Give the extent of all Plasmodium malariae-infected red blood cells.
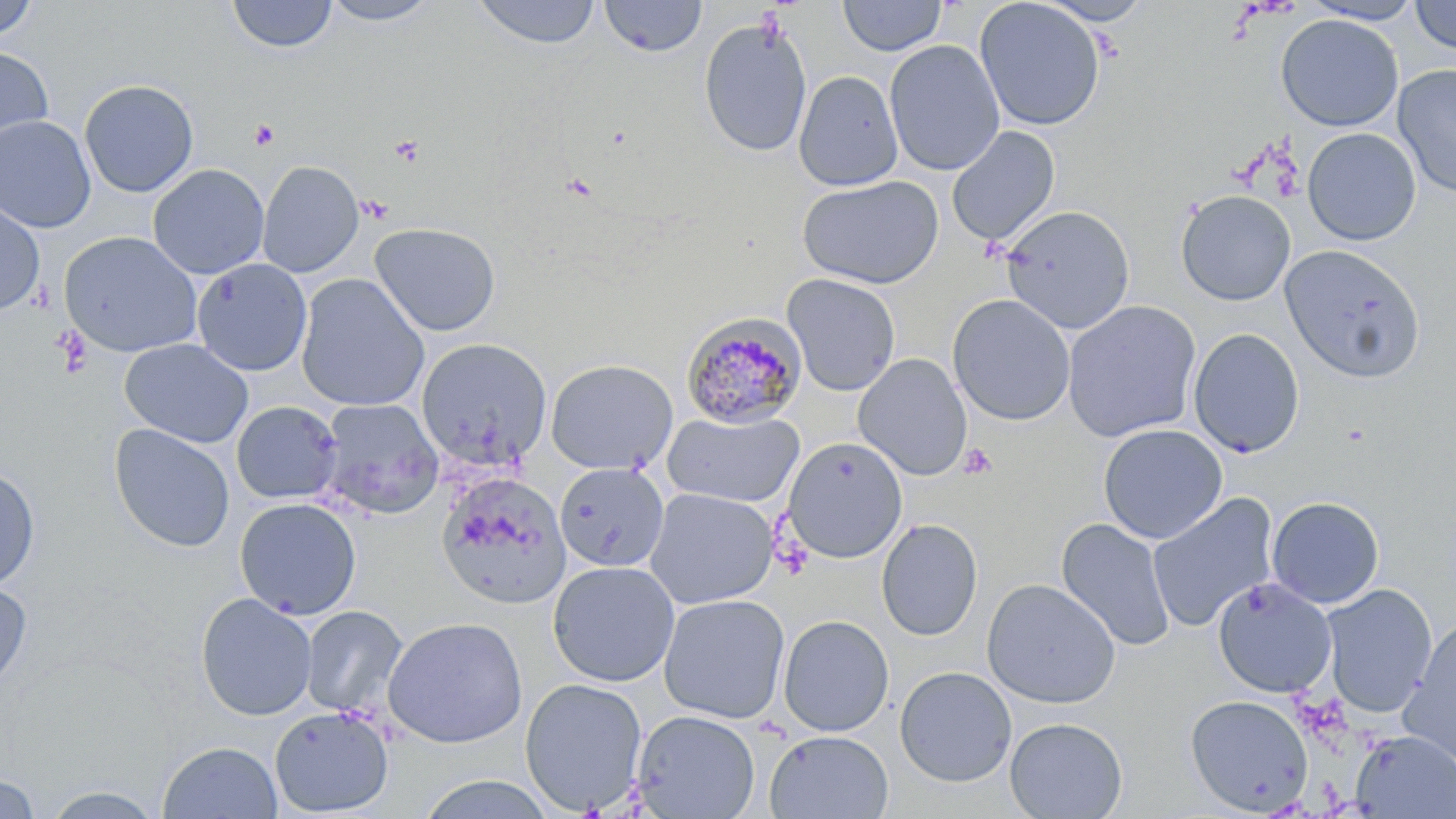

Approximate bounding boxes as (x1,y1)-(x2,y2) corner pairs in pixels.
Plasmodium malariae-infected red blood cells: (681,312)-(808,429).

Platelet locations: (249,119)-(280,150), (357,195)-(393,224), (958,443)-(998,479). Uninfected red blood cell locations: (0,0)-(40,42), (319,0)-(443,26), (598,0)-(708,58), (837,0)-(947,57), (974,0)-(1105,132), (1037,0)-(1155,25), (1301,0)-(1426,24), (226,1)-(338,53), (472,1)-(602,49), (1409,1)-(1456,54), (1275,14)-(1404,132), (698,17)-(813,158), (884,39)-(1005,176), (0,45)-(54,157), (1392,64)-(1456,200), (794,70)-(903,191), (79,79)-(199,197), (0,115)-(96,233), (946,126)-(1060,247), (1302,127)-(1421,245), (257,160)-(364,277), (148,164)-(269,279), (796,175)-(944,288), (1175,189)-(1296,306), (0,196)-(45,316), (1000,204)-(1136,334), (369,222)-(501,336), (59,231)-(203,358), (1281,244)-(1425,382), (191,258)-(312,376), (295,273)-(430,412), (782,273)-(901,396), (947,293)-(1076,426), (1063,300)-(1201,442), (1188,327)-(1305,457), (119,338)-(254,449), (416,338)-(552,469), (853,354)-(973,481), (545,359)-(678,475), (319,398)-(444,519), (231,401)-(342,504), (663,410)-(805,507), (108,423)-(235,553), (1098,424)-(1228,544), (782,437)-(908,563), (554,462)-(669,572), (0,465)-(40,590), (436,472)-(571,608), (644,487)-(779,609), (1147,493)-(1279,633), (1266,496)-(1384,608), (234,497)-(362,619), (876,518)-(983,641), (1056,518)-(1175,652), (547,560)-(680,687), (1212,577)-(1337,698), (982,579)-(1121,709), (0,580)-(32,690), (1319,584)-(1438,717), (195,592)-(318,721), (658,594)-(790,724), (300,605)-(407,717), (778,615)-(894,736), (382,616)-(528,748), (1401,617)-(1456,765), (894,666)-(1017,786), (519,678)-(648,815), (1185,694)-(1313,815), (269,706)-(394,817), (631,710)-(761,818), (1005,717)-(1127,819), (763,730)-(893,818), (1352,731)-(1456,818), (157,741)-(283,818), (0,773)-(41,818), (413,773)-(557,818), (38,784)-(168,818). Slide-level diagnosis: Plasmodium malariae. May-Grünwald-Giemsa-stained preparation. Light microscopy. Image is 1456×819 pixels. Thin blood film. Single field of view. 1000x magnification.